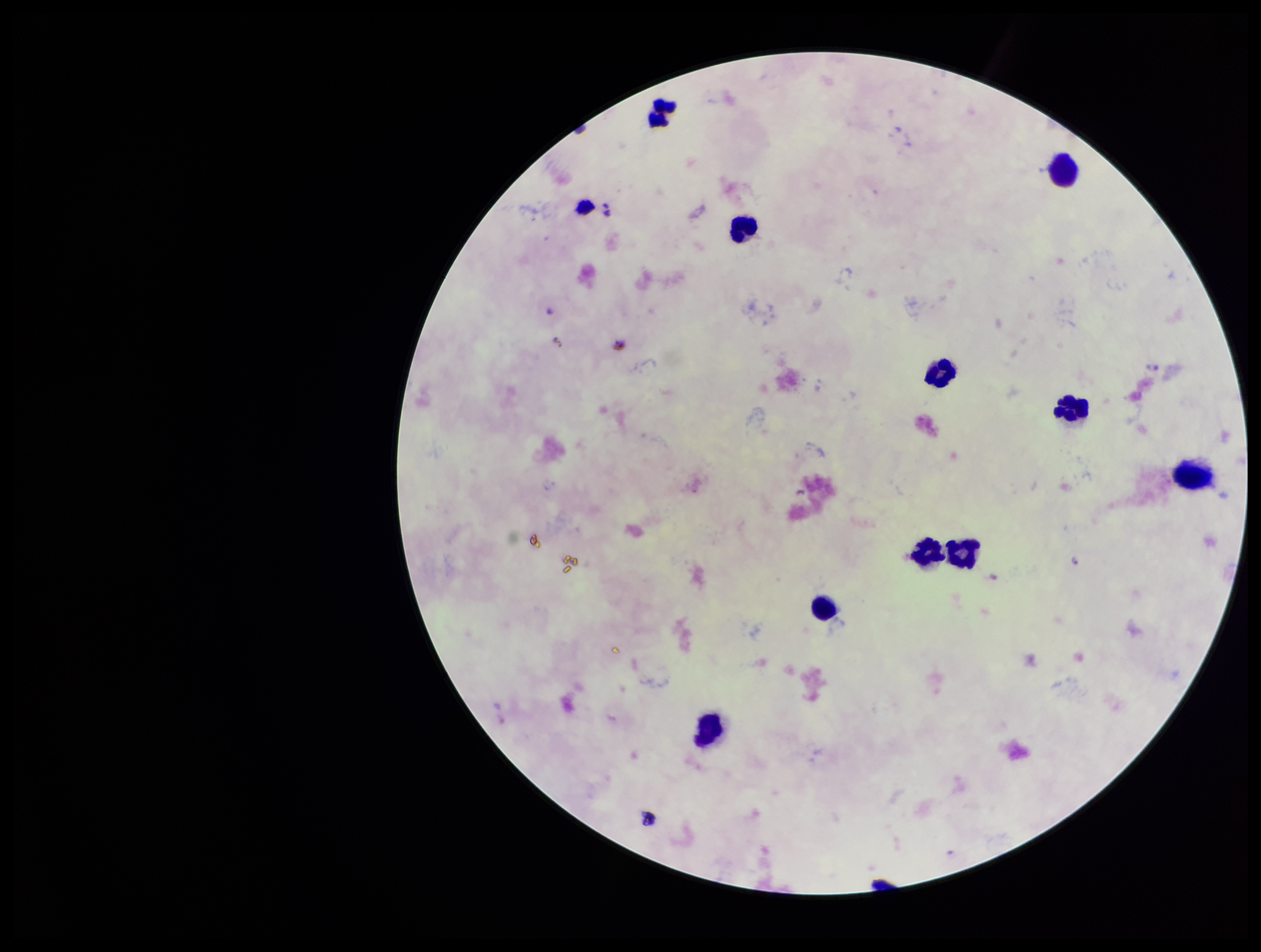 Leukocyte count: 11. Stained with Giemsa. Single field of view. Patient malaria status: positive. Plasmodium parasites: seen. Species reported for this patient: Plasmodium falciparum. Photographed through the microscope eyepiece with a smartphone camera. Preparation: thick. Parasite count: 2. Image is 1261×952 pixels.